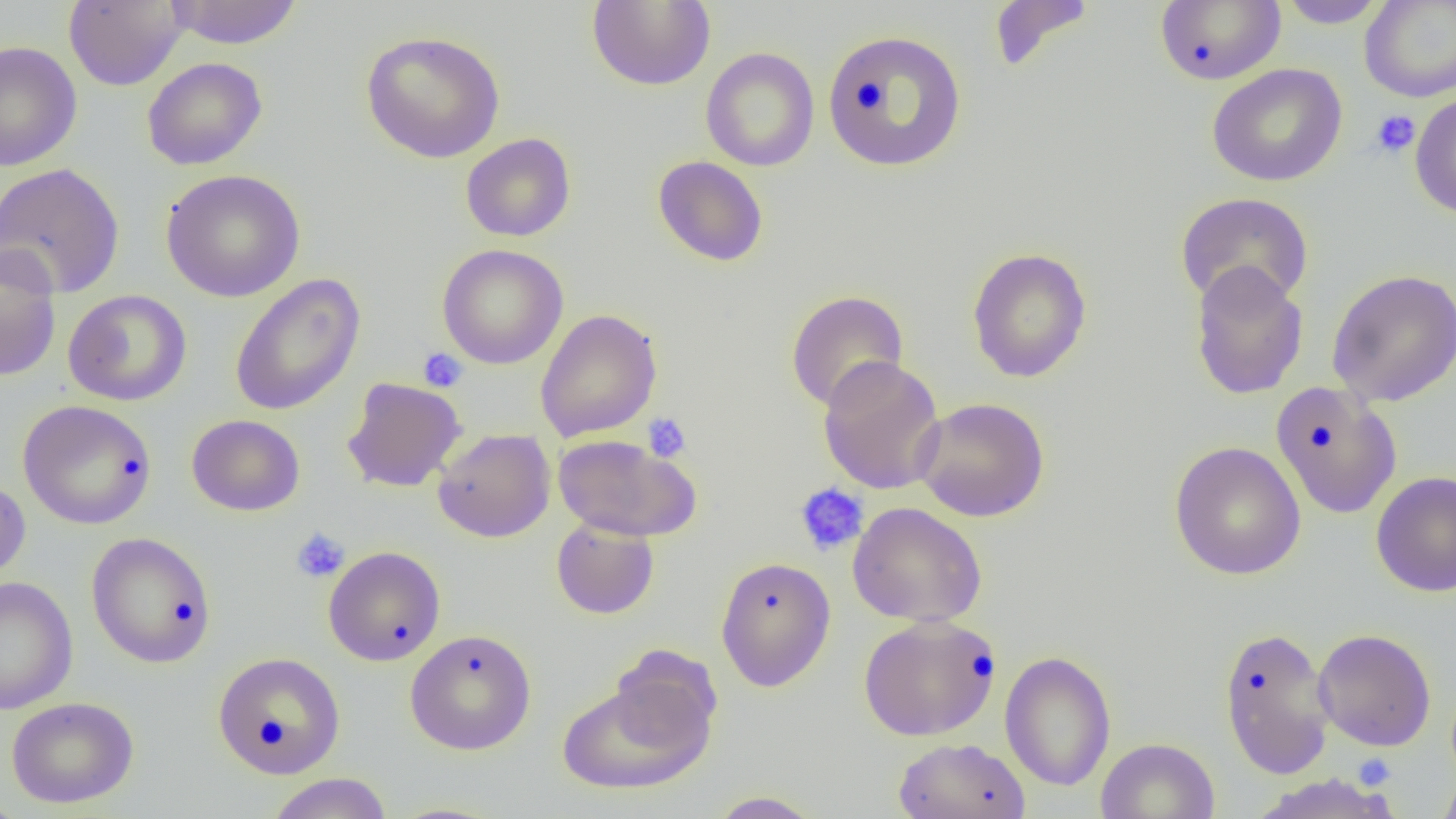
Summary:
  - Coordinate format: approximate bounding boxes as (x1,y1)-(x2,y2) corner pairs in pixels
  - Platelet locations: (1370,110)-(1421,157), (418,347)-(468,393), (642,413)-(692,462), (794,483)-(869,556), (291,527)-(350,583), (1353,752)-(1397,789)
  - Uninfected red blood cell locations: (63,0)-(188,90), (165,0)-(303,48), (988,0)-(1095,73), (1154,0)-(1286,86), (1276,0)-(1390,28), (1359,0)-(1456,103), (586,1)-(716,91), (822,28)-(968,173), (360,30)-(506,163), (0,40)-(82,172), (700,47)-(819,172), (142,56)-(268,171), (1207,63)-(1348,187), (1409,91)-(1456,219), (460,133)-(576,242), (652,155)-(768,267), (0,162)-(125,299), (160,168)-(306,302), (1175,191)-(1314,311), (0,244)-(62,382), (437,244)-(568,369), (966,247)-(1092,383), (1189,262)-(1309,400), (1326,268)-(1456,407), (229,273)-(366,417), (63,289)-(192,406), (785,289)-(909,413), (535,308)-(662,442), (817,355)-(946,495), (342,377)-(467,492), (1270,381)-(1402,519), (912,397)-(1050,522), (18,399)-(156,529), (187,414)-(305,516), (432,428)-(555,542), (553,435)-(699,541), (1168,441)-(1306,580), (1371,471)-(1456,597), (0,476)-(31,587), (847,502)-(987,627), (551,517)-(660,619), (85,532)-(217,669), (323,545)-(446,666), (715,556)-(836,692), (0,576)-(78,714), (863,619)-(1006,745), (1217,625)-(1335,779), (405,628)-(537,755), (1313,628)-(1437,751), (999,649)-(1117,792), (212,651)-(346,778), (557,670)-(717,796), (6,696)-(139,808), (893,737)-(1031,819), (1095,737)-(1220,819), (1437,771)-(1456,819), (266,773)-(394,819), (1248,773)-(1403,819), (707,790)-(825,818), (0,792)-(26,819)
  - Slide-level diagnosis: no evidence of blood parasites
  - Modality: light microscopy
  - Image size: 1456×819 pixels
  - Magnification: 1000x
  - Field of view: one of a larger specimen
  - Preparation: thin blood film